Give the preparation type.
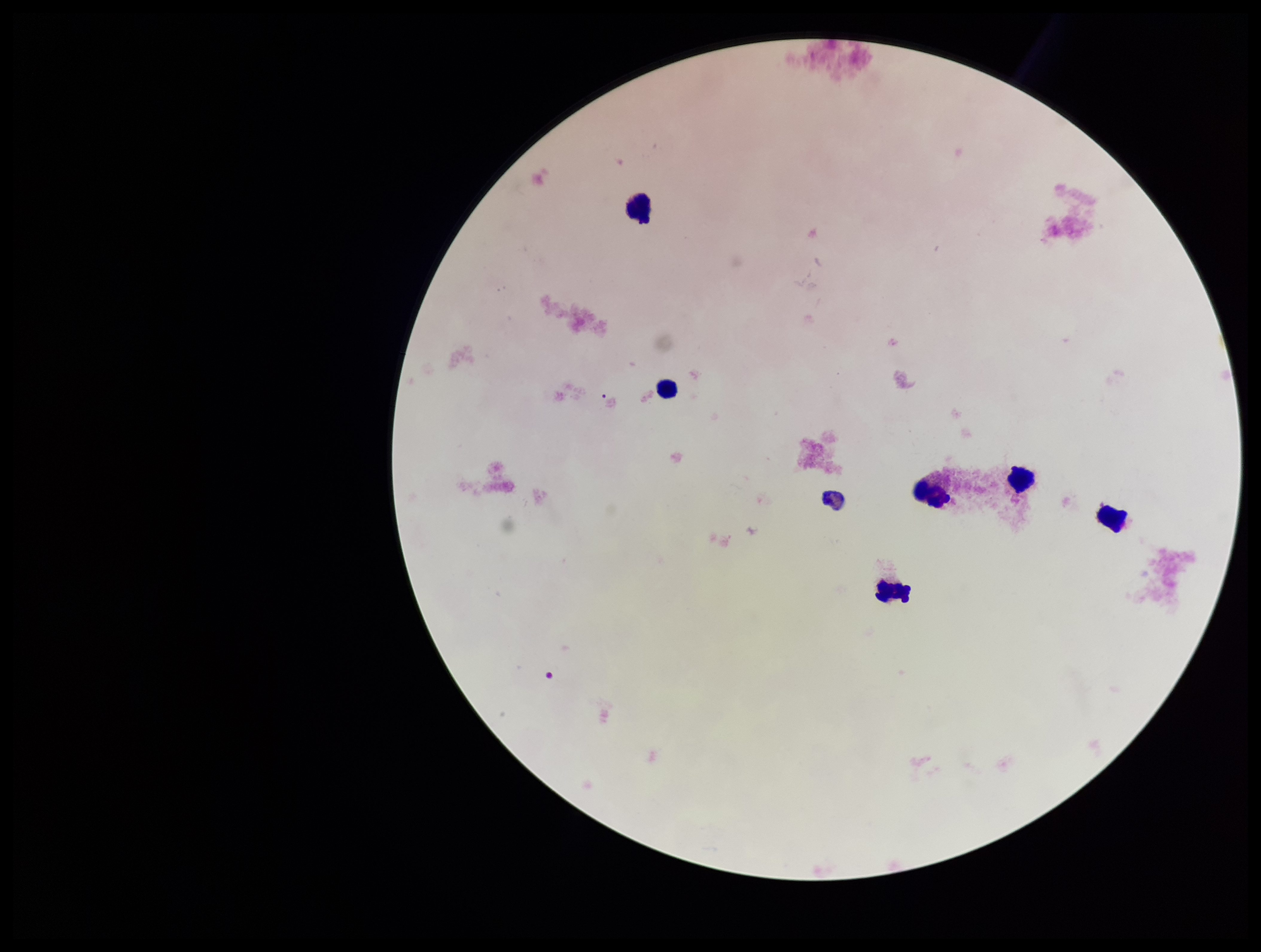

A thick smear.

patient malaria status = negative
parasite count = 0
capture = smartphone photograph through the microscope eyepiece
stain = Giemsa
Plasmodium parasites = none seen
leukocyte count = 6
field of view = one from this slide
image size = 1261×952 pixels